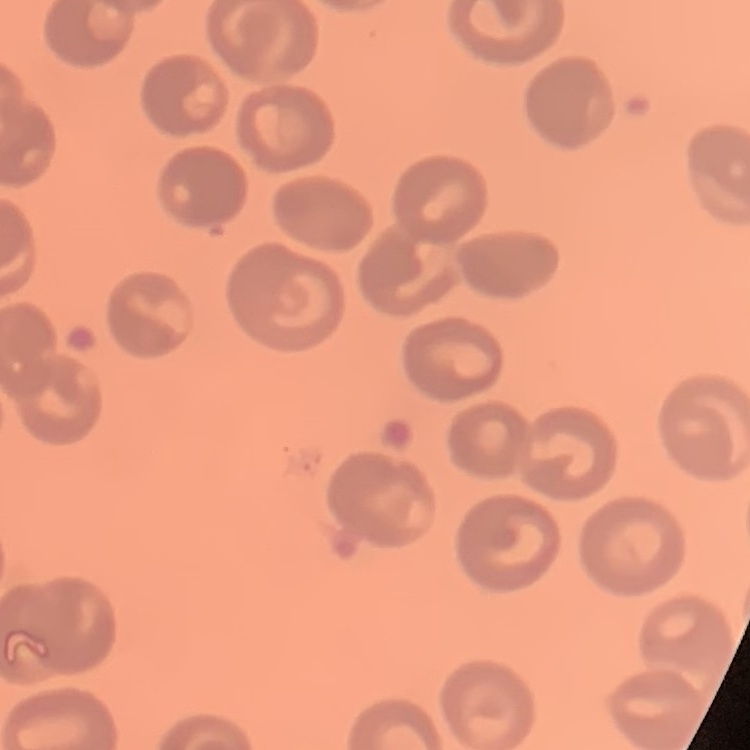

erythrocyte morphology = no rouleaux formation
stain = Field's or Giemsa
preparation = thin peripheral smear
image type = one tile cut from a larger photomicrograph